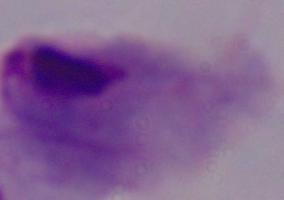 1000x magnification. A trichomonad is shown. Photomicrograph.